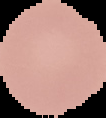

Summary:
  - Image type: segmented cell region on a black background
  - Result: no Plasmodium parasites detected
  - Image size: 106×118 pixels
  - Preparation: thin blood smear